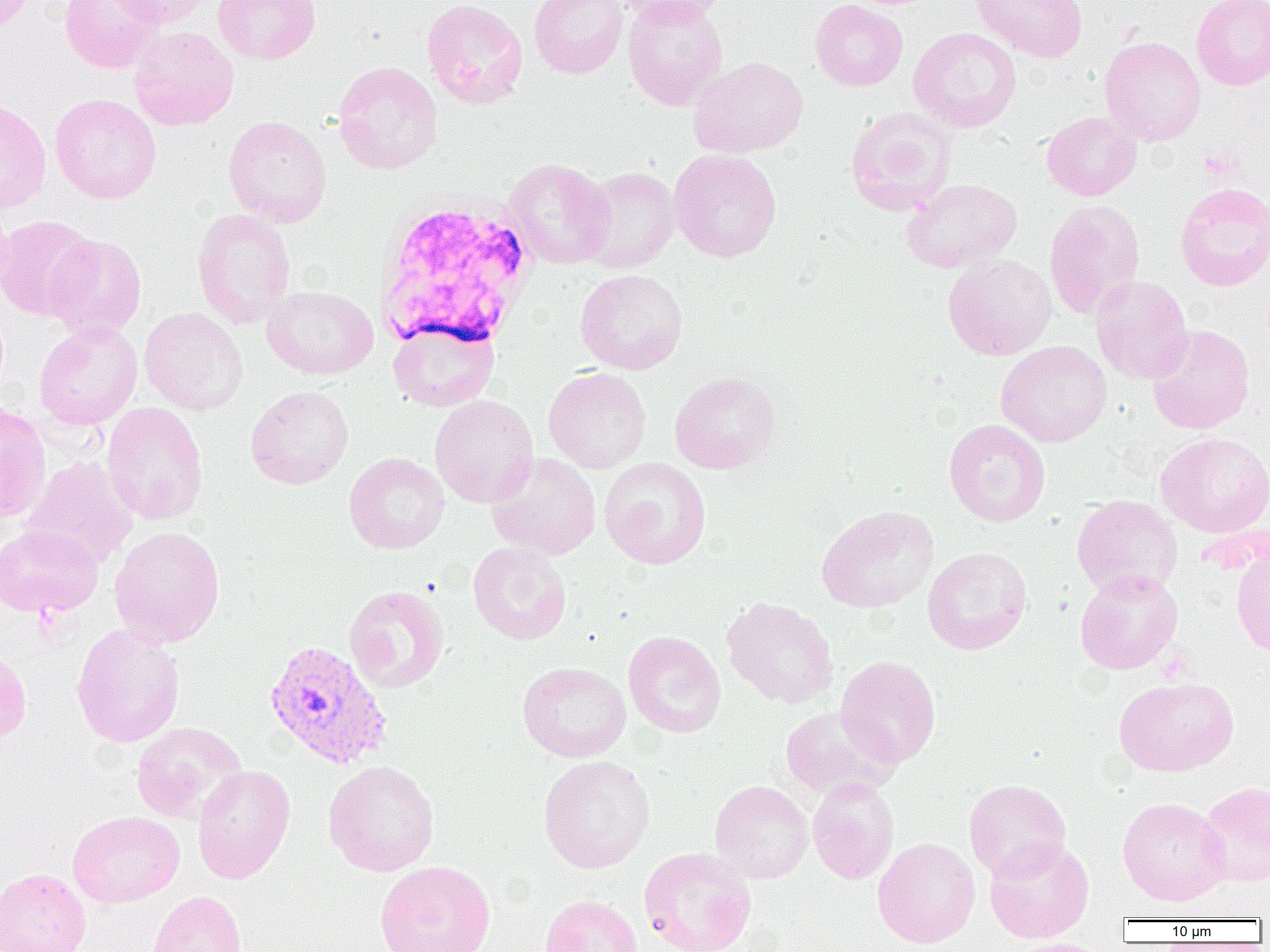
slide-level diagnosis = Plasmodium vivax
magnification = 1000x
image size = 1270×952 pixels
uninfected red blood cell locations = approximate bounding boxes as [x1, y1, x2, y2] in pixels: [0, 0, 38, 32], [59, 0, 165, 74], [106, 0, 214, 29], [213, 0, 320, 65], [422, 0, 528, 109], [529, 0, 628, 79], [614, 0, 731, 26], [622, 0, 728, 110], [810, 0, 908, 91], [971, 0, 1088, 62], [1191, 0, 1270, 91], [129, 26, 239, 131], [908, 27, 1022, 132], [1099, 36, 1206, 146], [688, 56, 808, 158], [333, 61, 443, 175], [50, 93, 162, 204], [0, 97, 52, 213], [845, 107, 957, 216], [1041, 111, 1141, 201], [224, 115, 331, 227], [669, 149, 782, 263], [502, 158, 616, 269], [579, 167, 680, 273], [901, 179, 1022, 273], [1174, 182, 1270, 291], [0, 199, 14, 298], [1043, 200, 1145, 320], [191, 208, 296, 328], [0, 215, 99, 321], [45, 234, 147, 341], [943, 254, 1057, 360], [575, 269, 688, 375], [1090, 275, 1193, 384], [262, 285, 379, 380], [139, 306, 248, 415], [34, 320, 142, 431], [387, 321, 499, 412], [1146, 324, 1255, 434], [996, 341, 1112, 447], [543, 367, 651, 473], [669, 371, 781, 474], [245, 385, 354, 490], [430, 395, 539, 508], [0, 402, 51, 523], [102, 402, 208, 526], [944, 419, 1051, 527], [1155, 432, 1270, 537], [344, 452, 450, 554], [487, 452, 602, 560], [21, 456, 138, 570], [599, 457, 711, 570], [1071, 495, 1183, 599], [816, 505, 939, 614], [0, 524, 103, 618], [109, 525, 225, 648], [468, 541, 572, 645], [922, 547, 1033, 654], [1231, 548, 1270, 660], [1074, 569, 1183, 675], [343, 584, 449, 694], [721, 597, 839, 709], [71, 624, 185, 748], [623, 630, 726, 738], [0, 645, 31, 746], [835, 655, 941, 767], [517, 661, 631, 763], [1114, 676, 1238, 777], [779, 706, 902, 800], [130, 722, 248, 824], [537, 755, 656, 873], [323, 760, 439, 876], [192, 765, 296, 884], [807, 778, 899, 884], [709, 779, 814, 883], [963, 779, 1072, 881], [1198, 781, 1270, 887], [1117, 797, 1231, 906], [67, 810, 184, 908], [872, 837, 981, 948], [984, 839, 1095, 943], [639, 848, 757, 952], [375, 860, 496, 952], [0, 868, 91, 952], [147, 890, 248, 952], [539, 895, 643, 952], [1006, 938, 1114, 952]
Plasmodium vivax-infected red blood cell locations = approximate bounding boxes as [x1, y1, x2, y2] in pixels: [262, 638, 394, 770]
field of view = single
preparation = thin blood smear
platelet locations = approximate bounding boxes as [x1, y1, x2, y2] in pixels: [1199, 149, 1241, 182]
white blood cell locations = approximate bounding boxes as [x1, y1, x2, y2] in pixels: [380, 189, 538, 359]
modality = optical microscopy